Report the malaria status of this cell.
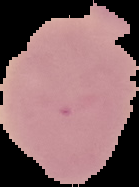

Uninfected.

image type = segmented cell region with the area outside set to black
preparation = thin blood smear
image size = 139×187 pixels